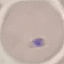

Summary:
  - Malaria status: uninfected
  - Stain: Giemsa
  - Capture: smartphone through the microscope eyepiece
  - Preparation: thin blood film
  - Image type: cell patch, automatically extracted from a larger field of view and resized to 64 × 64 pixels